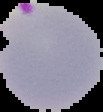

preparation: thin blood smear
image_type: cell region segmented out of the field of view; surrounding area masked to black
malaria_status: parasitized
image_size: 103×112 pixels